Assess this cell for malaria.
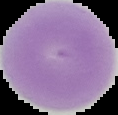

It is uninfected.

Summary:
  - Image size: 118×115 pixels
  - Image type: cell region segmented out of the field of view; surrounding area masked to black
  - Preparation: thin blood smear